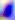
{
  "identification": "Toxoplasma gondii",
  "magnification": "400x",
  "modality": "photomicrograph"
}